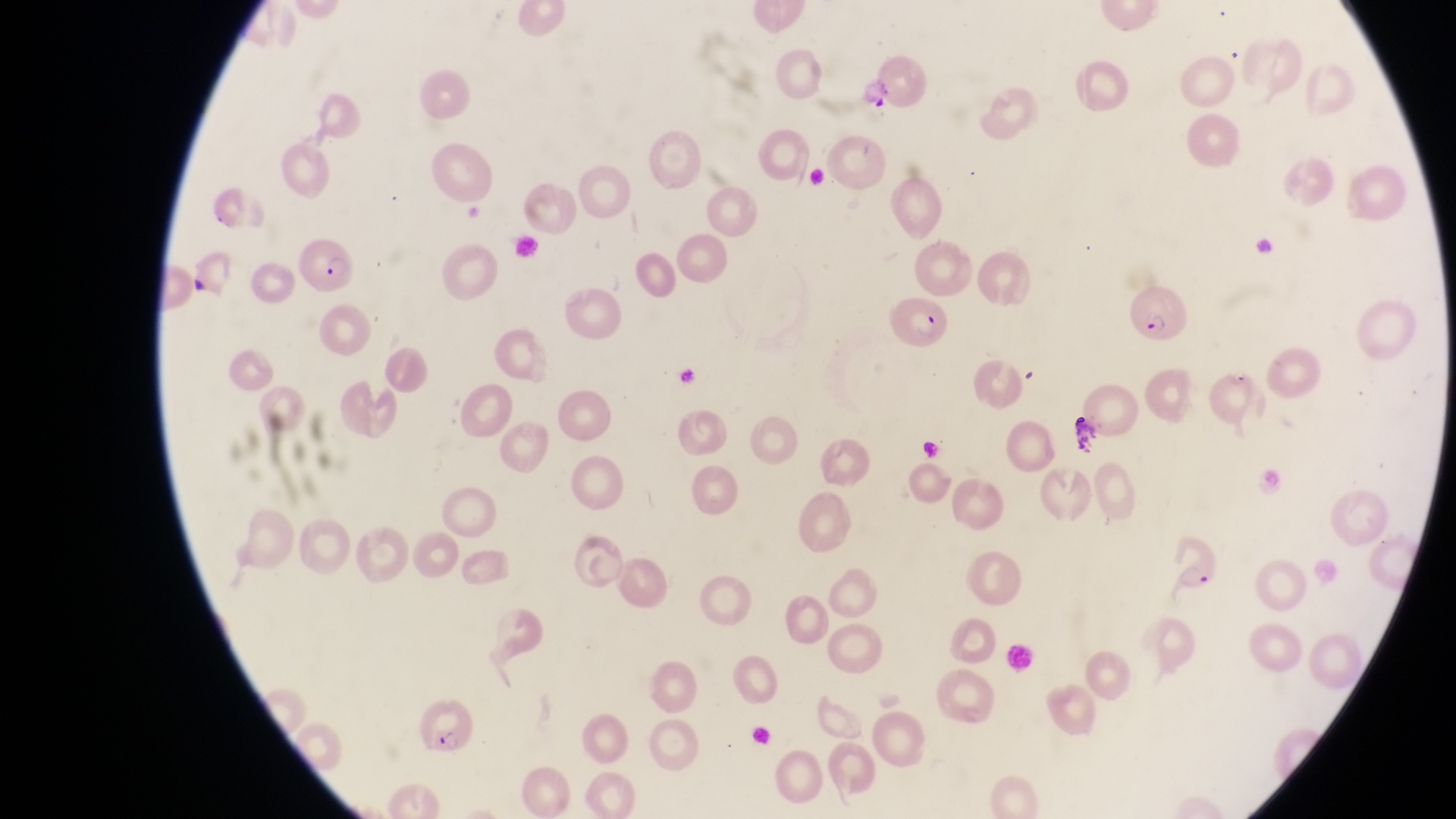
field_of_view: single
magnification: 1000x
parasitised_red_blood_cell_locations: 'approximate bounding boxes as [left, top, right, bottom] in pixels: [291, 238, 358, 299], [1129, 288, 1202, 360], [885, 291, 957, 355], [1171, 525, 1230, 594], [407, 700, 480, 759]'
preparation: thin blood film
capture: smartphone photograph through the eyepiece of an Olympus CX-23 microscope
country: Uganda
image_size: 1456×819 pixels